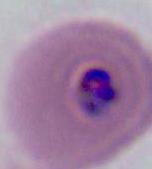 Photomicrograph. A Plasmodium parasite is shown. Captured at either 400x or 1000x magnification.